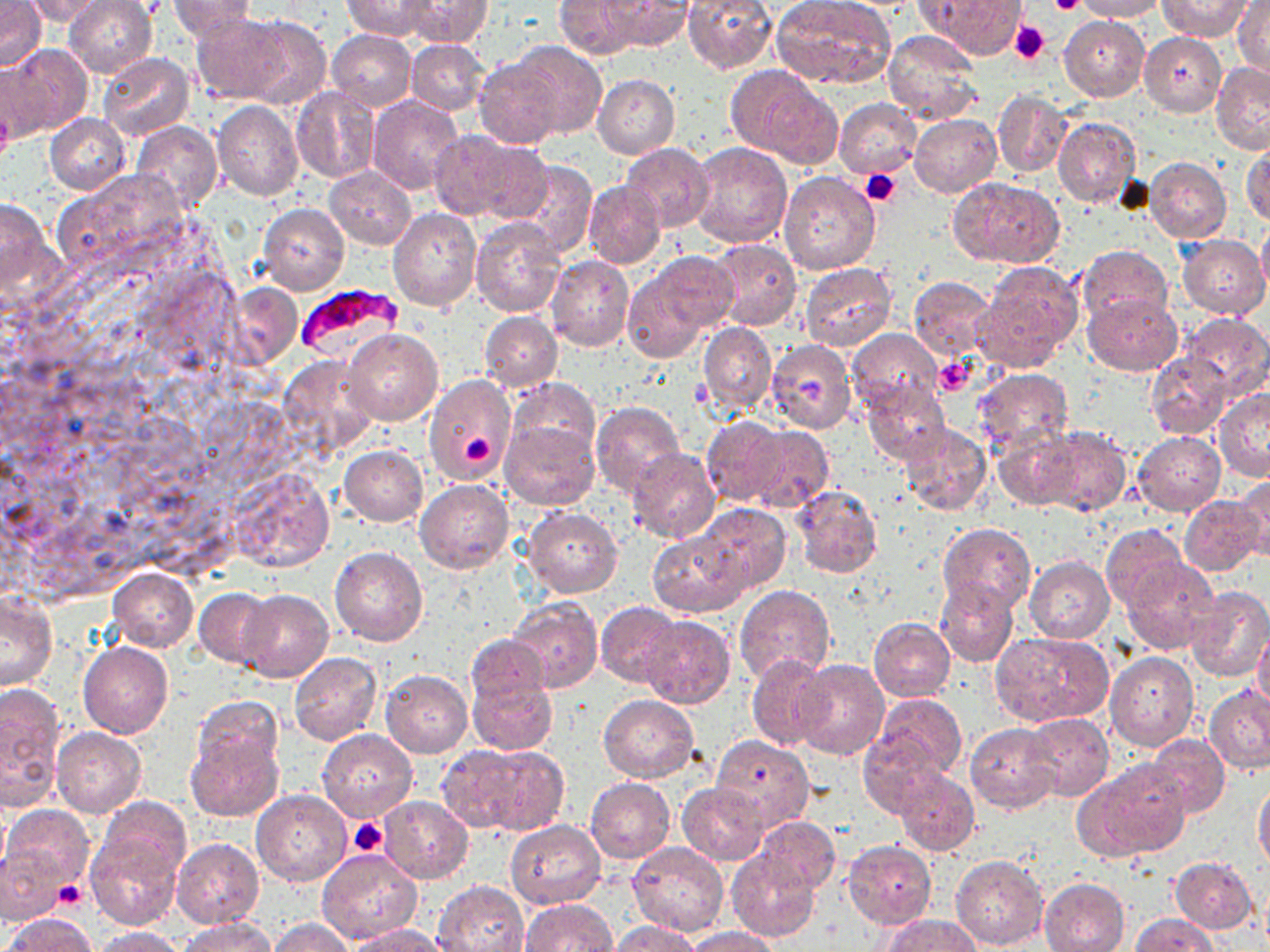 Approximate bounding boxes as (x1, y1, x2, y2) in pixels. Plasmodium falciparum-infected red blood cell locations: (295, 285, 405, 362). Uninfected red blood cell locations: (0, 0, 43, 72), (64, 0, 158, 78), (167, 0, 259, 41), (343, 0, 441, 38), (401, 0, 492, 48), (683, 0, 777, 75), (770, 0, 896, 88), (925, 0, 1026, 58), (1070, 0, 1167, 21), (1158, 0, 1251, 41), (22, 1, 111, 24), (554, 1, 642, 59), (603, 1, 691, 51), (1233, 1, 1269, 77), (192, 11, 291, 103), (232, 14, 332, 109), (1058, 15, 1149, 102), (326, 29, 416, 110), (882, 29, 982, 123), (1139, 32, 1226, 116), (406, 38, 489, 116), (511, 40, 606, 137), (2, 42, 91, 135), (97, 52, 194, 142), (474, 58, 564, 148), (0, 60, 52, 145), (1211, 60, 1270, 153), (728, 66, 837, 165), (593, 74, 680, 158), (292, 87, 381, 183), (992, 90, 1072, 177), (367, 95, 464, 194), (834, 98, 921, 180), (212, 102, 303, 200), (45, 113, 130, 195), (910, 114, 1001, 197), (1053, 116, 1142, 209), (131, 120, 222, 215), (428, 130, 515, 219), (468, 141, 553, 224), (1243, 141, 1270, 227), (689, 142, 794, 249), (620, 143, 714, 231), (692, 155, 883, 258), (1144, 157, 1231, 242), (504, 160, 598, 258), (324, 166, 416, 250), (778, 170, 880, 275), (950, 178, 1063, 266), (583, 181, 665, 271), (0, 197, 57, 299), (257, 204, 349, 295), (387, 207, 481, 311), (1257, 218, 1270, 302), (469, 219, 566, 317), (1178, 235, 1269, 319), (709, 238, 802, 331), (1077, 245, 1172, 327), (546, 255, 635, 353), (623, 255, 730, 358), (974, 261, 1083, 371), (799, 262, 896, 350), (908, 277, 996, 359), (1081, 292, 1182, 375), (479, 312, 561, 392), (1178, 312, 1270, 396), (699, 323, 776, 413), (847, 328, 941, 417), (343, 329, 442, 424), (767, 339, 855, 434), (1148, 352, 1234, 440), (973, 369, 1074, 458), (423, 374, 514, 484), (863, 379, 951, 468), (506, 380, 600, 462), (1212, 388, 1270, 481), (591, 400, 687, 502), (703, 416, 789, 506), (500, 419, 599, 510), (898, 422, 990, 516), (743, 425, 834, 511), (1033, 426, 1132, 517), (994, 428, 1078, 509), (1133, 432, 1226, 515), (340, 445, 428, 526), (626, 449, 721, 544), (1235, 475, 1270, 562), (415, 480, 513, 573), (791, 484, 882, 579), (1179, 495, 1267, 577), (694, 503, 791, 593), (524, 506, 622, 597), (939, 524, 1036, 612), (1102, 525, 1187, 611), (649, 531, 748, 618), (329, 547, 427, 646), (1024, 556, 1114, 643), (1121, 558, 1219, 654), (108, 567, 198, 650), (934, 577, 1017, 668), (734, 584, 837, 684), (1183, 586, 1270, 682), (195, 587, 278, 668), (239, 590, 333, 683), (0, 592, 57, 690), (506, 597, 603, 693), (597, 602, 684, 687), (640, 615, 734, 709), (868, 617, 956, 701), (1253, 625, 1270, 717), (989, 629, 1114, 727), (466, 633, 550, 709), (78, 643, 171, 737), (288, 652, 383, 745), (1104, 653, 1199, 750), (747, 655, 835, 750), (795, 661, 888, 759), (381, 671, 473, 757), (467, 674, 558, 754), (0, 684, 66, 809), (1204, 685, 1270, 774), (873, 693, 966, 779), (599, 694, 698, 781), (193, 695, 282, 775), (1022, 713, 1114, 801), (966, 723, 1059, 814), (51, 727, 146, 817), (185, 729, 283, 821), (317, 729, 416, 820), (858, 733, 944, 818), (1144, 734, 1229, 818), (712, 736, 813, 831), (441, 743, 566, 835), (1075, 758, 1193, 860), (895, 768, 979, 855), (585, 778, 675, 863), (1253, 779, 1270, 872), (677, 783, 770, 865), (250, 789, 352, 886), (380, 796, 473, 883), (95, 798, 191, 885), (3, 804, 94, 890), (756, 818, 840, 893), (506, 820, 606, 909), (86, 833, 183, 930), (172, 838, 263, 928), (844, 840, 937, 929), (627, 842, 729, 936), (0, 844, 66, 927), (316, 849, 424, 946), (727, 849, 820, 941), (949, 854, 1049, 949), (1169, 856, 1258, 934), (1040, 877, 1129, 952), (433, 880, 528, 952), (519, 899, 617, 952), (4, 913, 98, 951), (1129, 913, 1219, 951), (882, 914, 981, 952), (177, 918, 278, 952), (269, 918, 356, 952), (608, 920, 699, 952), (348, 924, 452, 952), (90, 926, 189, 951), (685, 927, 779, 952). Platelet locations: (1047, 0, 1085, 13), (1009, 21, 1049, 64), (0, 104, 15, 162), (860, 169, 899, 206), (934, 355, 976, 396), (462, 435, 495, 471), (350, 818, 387, 857), (54, 880, 86, 910). Slide-level diagnosis: Plasmodium falciparum. May-Grünwald-Giemsa-stained preparation. 1000x magnification. Image is 1270×952 pixels. Thin blood smear. Optical microscopy. Single field of view.